Name the parasite shown.
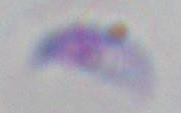

This is Toxoplasma gondii.

1000x magnification. Micrograph.